Comment on the morphology of the red blood cells.
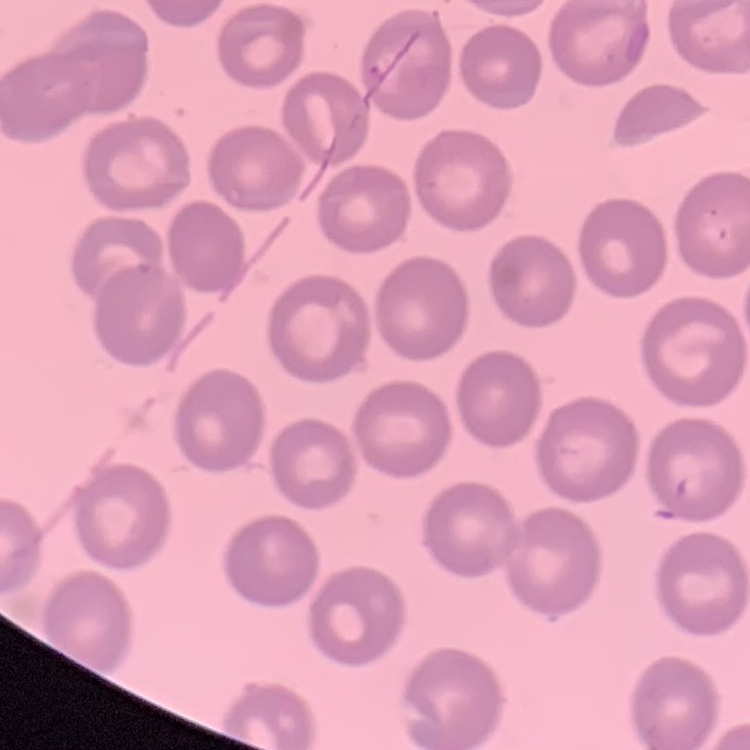

No rouleaux formation.

image type = square crop of a larger photomicrograph
preparation = thin blood smear
stain = Field's or Giemsa